Name the parasite shown.
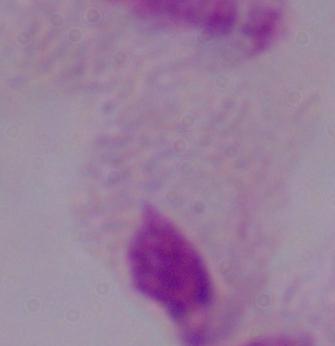

A trichomonad.

Photomicrograph. 1000x magnification.